Report the malaria status of this cell.
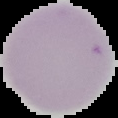

Uninfected.

Summary:
  - Image size: 118×118 pixels
  - Preparation: thin blood film
  - Image type: segmented cell region on a black background